Name the blood parasite species.
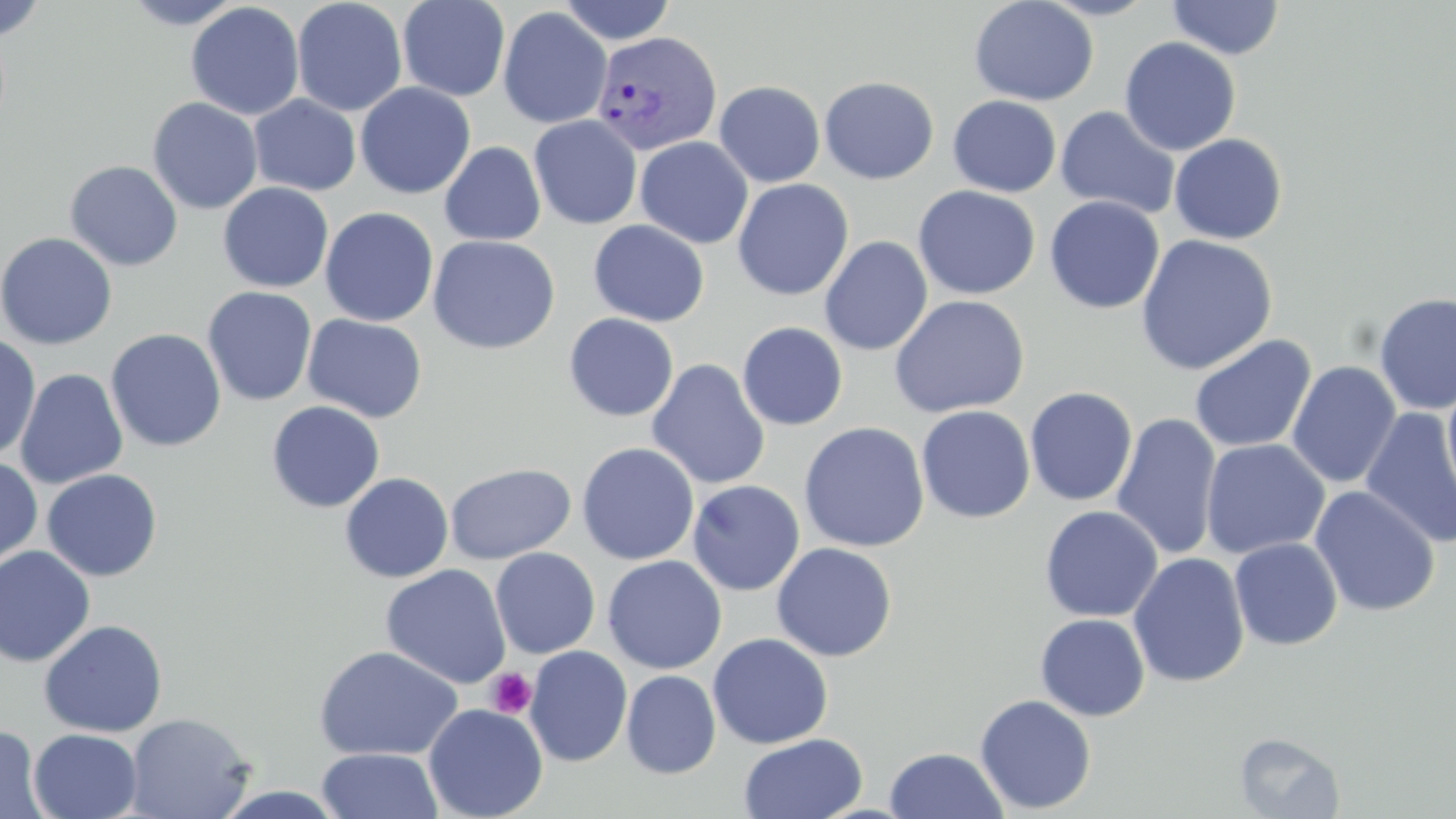

Plasmodium vivax.

field_of_view: single
image_size: 1456×819 pixels
platelet_locations: 'approximate bounding boxes as (x1, y1, x2, y2) in pixels: (486, 669, 536, 718)'
magnification: 1000x
uninfected_red_blood_cell_locations: 'approximate bounding boxes as (x1, y1, x2, y2) in pixels: (121, 0, 247, 29), (292, 0, 408, 117), (397, 0, 510, 101), (557, 0, 676, 45), (968, 0, 1099, 106), (1037, 0, 1159, 21), (0, 1, 48, 41), (1166, 1, 1285, 60), (185, 2, 304, 120), (497, 6, 612, 129), (1119, 37, 1241, 156), (819, 76, 939, 184), (714, 80, 826, 187), (355, 82, 476, 199), (248, 95, 361, 196), (948, 95, 1061, 197), (147, 96, 263, 215), (1054, 105, 1181, 219), (529, 115, 642, 229), (1169, 133, 1288, 245), (635, 136, 754, 249), (440, 141, 546, 246), (65, 160, 183, 271), (732, 179, 853, 301), (218, 182, 334, 293), (913, 186, 1041, 299), (1044, 196, 1165, 314), (319, 206, 439, 327), (588, 220, 710, 327), (0, 232, 118, 350), (1135, 234, 1278, 375), (427, 235, 560, 354), (819, 236, 933, 355), (202, 286, 318, 407), (1374, 292, 1456, 415), (889, 295, 1030, 417), (564, 313, 679, 422), (303, 314, 427, 423), (737, 322, 848, 430), (106, 328, 226, 452), (0, 333, 42, 462), (1189, 334, 1317, 453), (647, 359, 770, 490), (1286, 360, 1401, 489), (13, 367, 128, 490), (1442, 374, 1456, 513), (1024, 386, 1138, 507), (266, 400, 385, 513), (916, 405, 1035, 523), (1360, 408, 1456, 549), (1111, 412, 1223, 561), (799, 421, 929, 552), (1201, 439, 1330, 559), (577, 442, 699, 565), (0, 456, 43, 573), (445, 462, 576, 565), (41, 469, 163, 581), (339, 472, 454, 583), (686, 479, 805, 596), (1310, 485, 1440, 617), (1039, 505, 1163, 623), (1229, 537, 1343, 650), (771, 542, 897, 662), (0, 545, 96, 666), (490, 547, 600, 659), (1128, 552, 1250, 688), (602, 555, 727, 674), (380, 564, 511, 690), (1035, 613, 1150, 721), (38, 619, 169, 737), (707, 633, 834, 749), (313, 645, 464, 761), (524, 645, 632, 767), (621, 669, 721, 779), (974, 694, 1096, 814), (423, 703, 548, 818), (125, 712, 255, 819), (0, 724, 50, 819), (28, 728, 142, 818), (739, 732, 867, 819), (1234, 732, 1345, 818), (884, 747, 1009, 818), (317, 748, 443, 819)'
stain: May-Grünwald-Giemsa
preparation: thin blood film
modality: optical microscopy
plasmodium_vivax_infected_red_blood_cell_locations: 'approximate bounding boxes as (x1, y1, x2, y2) in pixels: (592, 31, 723, 156)'